Comment on the morphology of the erythrocytes.
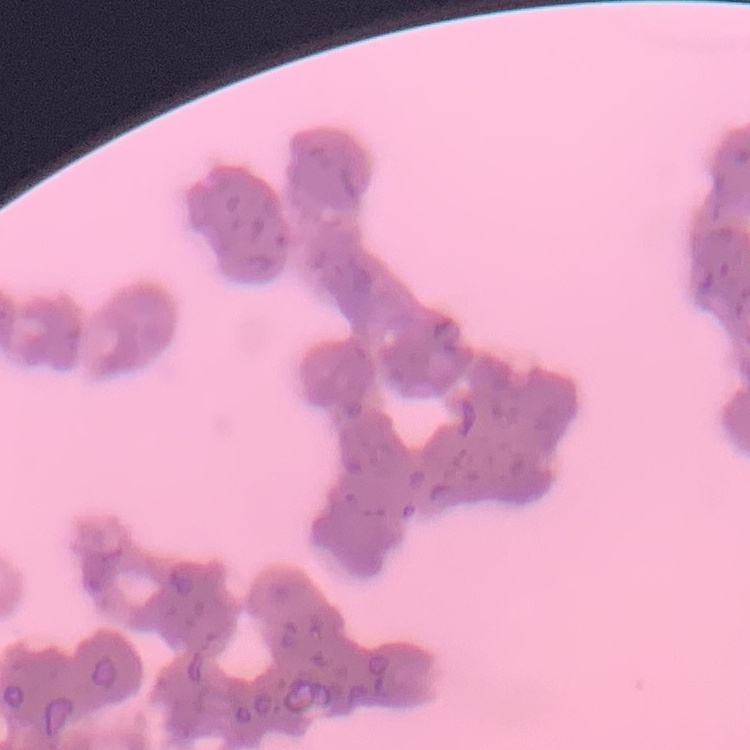

Rouleaux formation.

stain: Field's or Giemsa
preparation: thin blood film
image_type: one tile cut from a larger photomicrograph